Describe the morphology of the red blood cells.
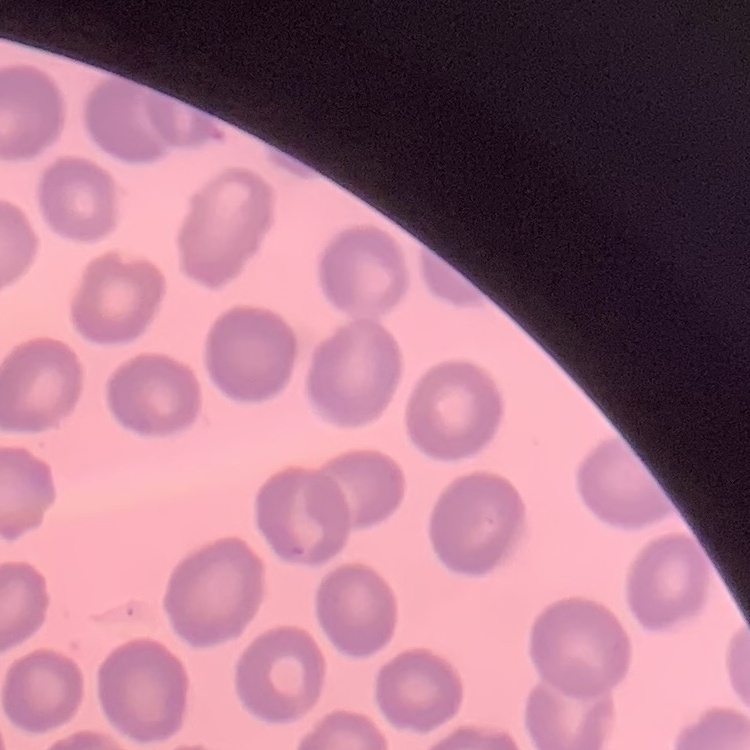

They show no rouleaux formation.

{
  "image_type": "one tile cut from a larger photomicrograph",
  "preparation": "thin blood film",
  "stain": "Field's or Giemsa"
}